Classify this cell by malaria status.
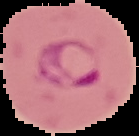
Parasitized.

Summary:
  - Preparation: thin blood smear
  - Image size: 139×136 pixels
  - Image type: segmented cell region on a black background